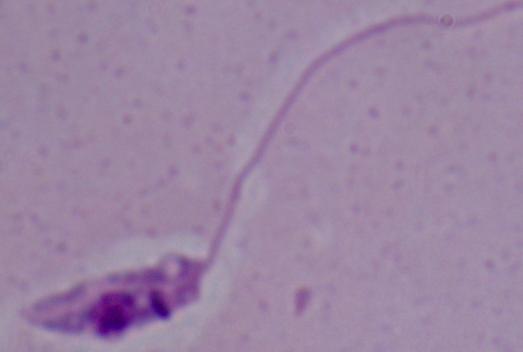
A Leishmania parasite is shown. Captured at 1000x magnification. Micrograph.